State which parasite is depicted.
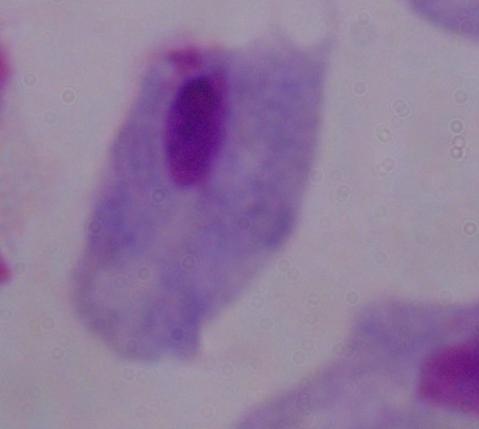
A trichomonad.

{
  "magnification": "1000x",
  "modality": "micrograph"
}